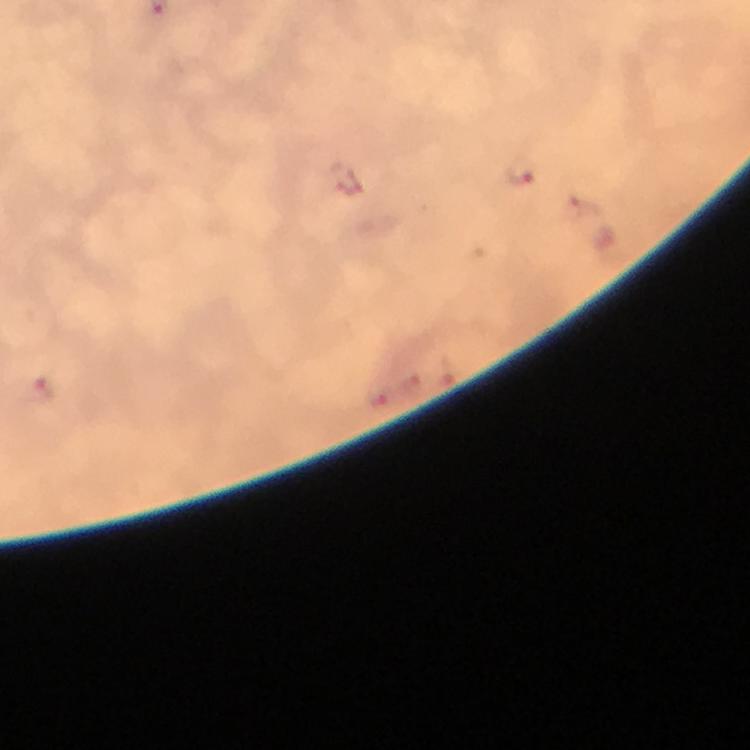

Approximate centers as [x, y] in pixels. Malaria parasite locations: [522, 171], [582, 206], [41, 389], [378, 397]. Cropped region of a single field of view. From a malaria diagnostic workup. Giemsa-stained preparation. Immersion oil was used. Image is 750×750 pixels. Thick blood film. Photographed through the microscope with a smartphone camera. At 100x magnification.